Identify the parasite.
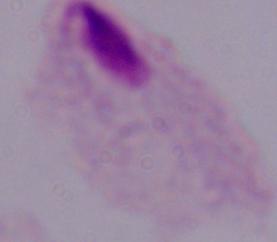

This is a trichomonad.

Captured at 1000x magnification. Photomicrograph.